Describe the morphology of the red blood cells.
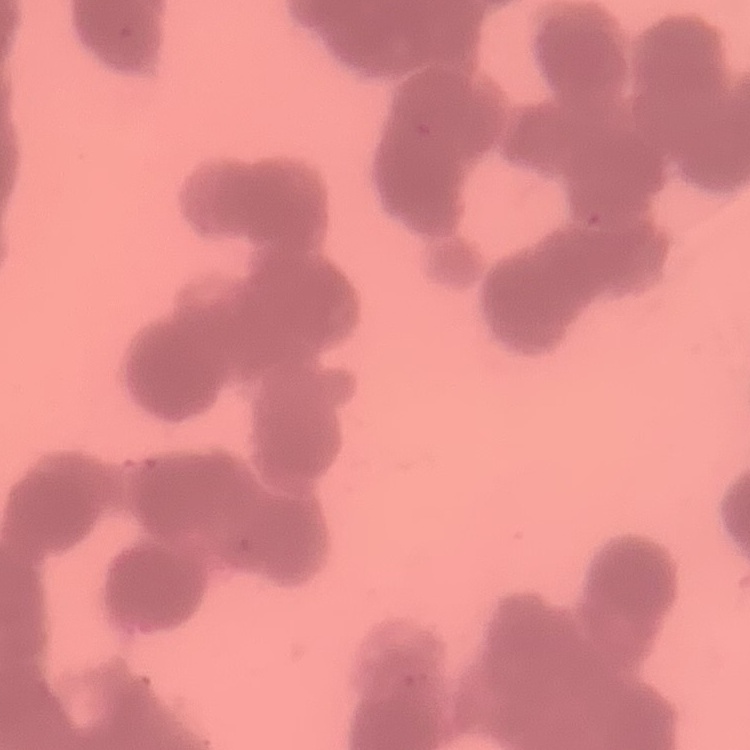
They show rouleaux formation.

One tile cut from a larger photomicrograph. Field's or Giemsa stain. Thin blood smear.